Outline each blood parasite and name the species.
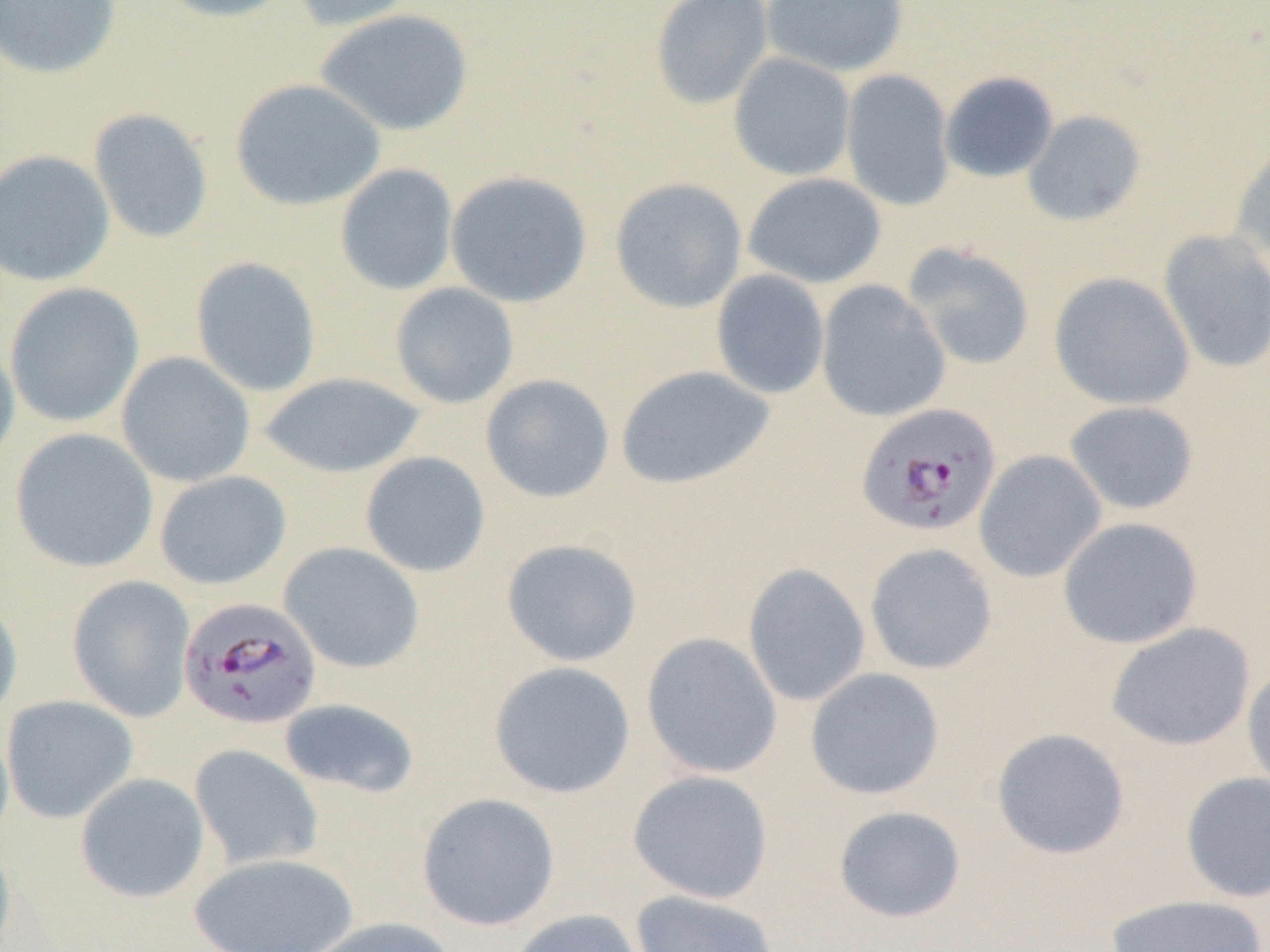

Approximate bounding boxes as (x1,y1)-(x2,y2) corner pairs in pixels.
Plasmodium falciparum-infected red blood cells: (855,403)-(1002,538), (177,597)-(322,731).
No Plasmodium ovale, Plasmodium malariae, Plasmodium vivax, Babesia divergens, or Trypanosoma brucei observed.

Uninfected red blood cell locations: (0,0)-(122,80), (153,0)-(300,23), (289,0)-(424,32), (650,0)-(774,109), (761,0)-(910,78), (314,8)-(475,138), (728,52)-(856,181), (841,69)-(956,211), (939,72)-(1058,183), (229,78)-(386,212), (88,108)-(214,244), (1022,110)-(1146,227), (1229,137)-(1270,266), (0,149)-(115,287), (334,163)-(459,296), (445,170)-(593,308), (742,173)-(887,289), (609,177)-(748,313), (1158,230)-(1270,374), (904,243)-(1035,371), (190,256)-(322,398), (710,270)-(830,399), (1048,271)-(1196,411), (816,280)-(950,422), (5,282)-(144,428), (389,282)-(520,409), (0,339)-(20,474), (116,351)-(255,488), (615,365)-(775,491), (259,371)-(426,478), (480,373)-(615,503), (1064,400)-(1200,515), (9,428)-(159,573), (974,449)-(1107,583), (360,451)-(491,578), (154,470)-(292,590), (1057,516)-(1204,649), (501,537)-(643,667), (280,542)-(425,674), (863,542)-(999,675), (742,563)-(871,707), (67,575)-(196,722), (0,594)-(23,728), (1105,621)-(1256,752), (640,632)-(783,779), (487,661)-(636,798), (1242,664)-(1270,799), (805,667)-(946,801), (1,695)-(139,824), (278,698)-(420,798), (0,718)-(15,848), (990,727)-(1131,861), (189,744)-(324,871), (627,769)-(775,904), (1180,771)-(1270,902), (75,772)-(210,904), (415,792)-(561,931), (831,805)-(968,924), (0,829)-(15,950), (188,852)-(359,951), (629,889)-(780,952), (1104,894)-(1268,952), (507,908)-(646,952), (297,917)-(459,952). Slide-level diagnosis: Plasmodium falciparum. Light microscopy. Single field of view. Captured at 1000x magnification. Image is 1270×952 pixels. Thin blood smear.